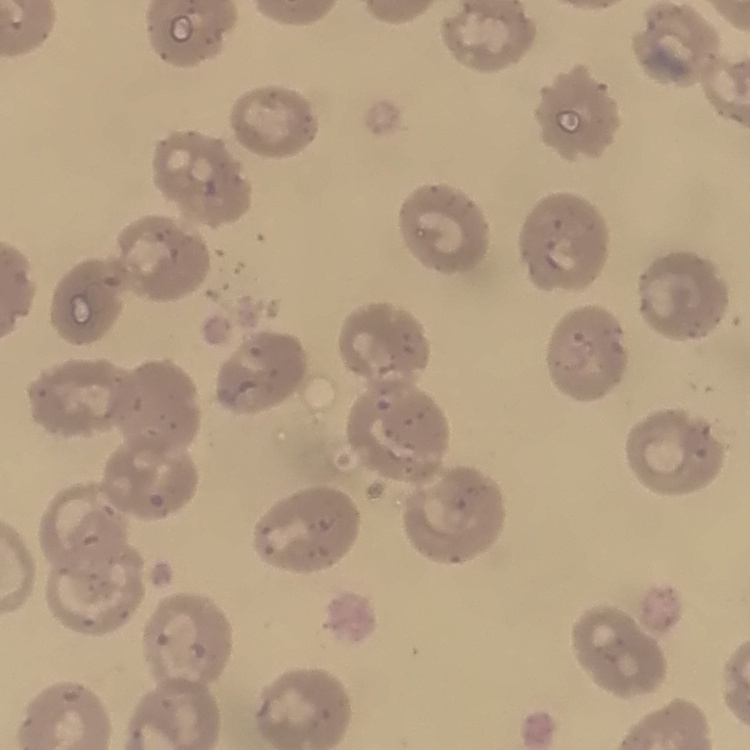

Summary:
  - Erythrocyte morphology: no rouleaux formation
  - Stain: Field's or Giemsa
  - Image type: one tile cut from a larger photomicrograph
  - Preparation: thin peripheral smear